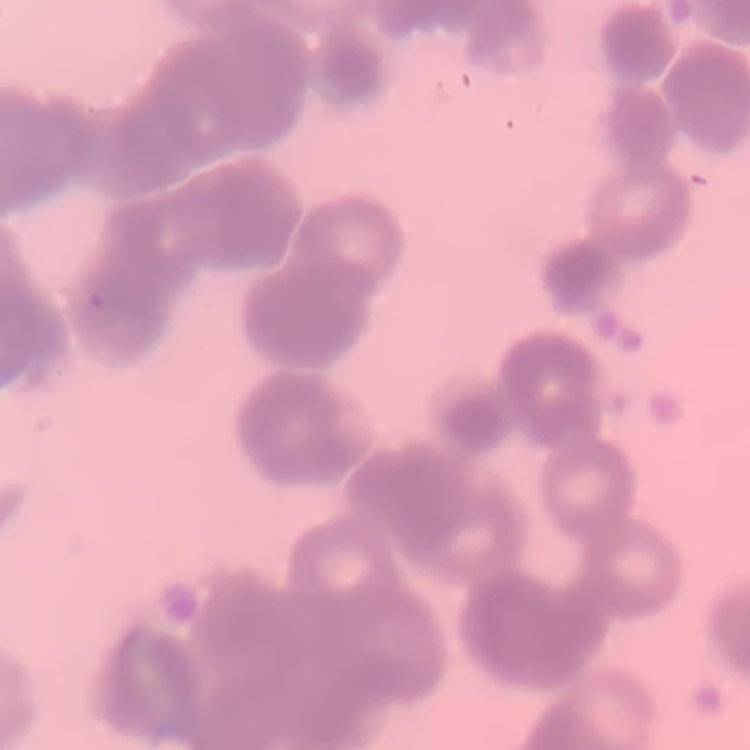
erythrocyte morphology = rouleaux formation
preparation = thin peripheral smear
stain = Field's or Giemsa
image type = one tile cut from a larger photomicrograph